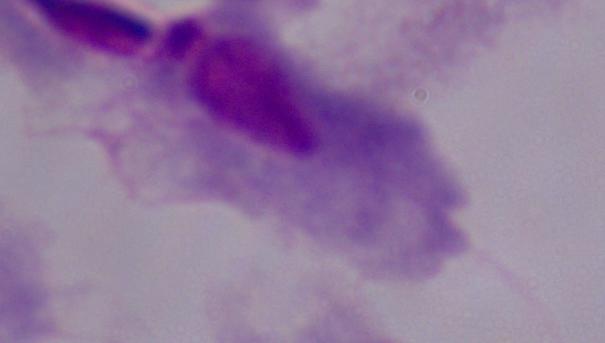
{
  "modality": "photomicrograph",
  "magnification": "1000x",
  "identification": "trichomonad"
}